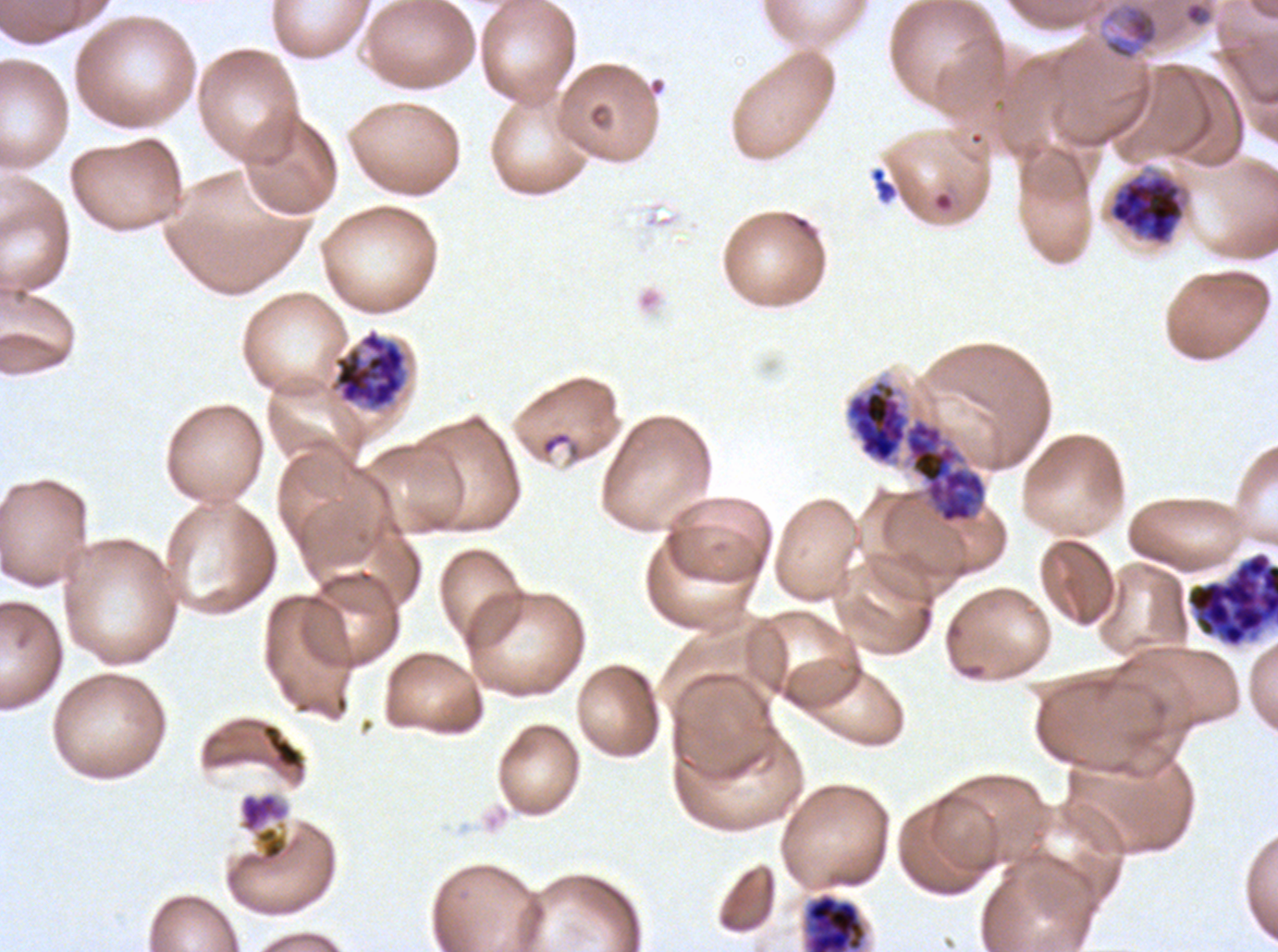 Approximate bounding boxes as (x1, y1, x2, y2) in pixels. Segmenter locations: (1185, 550, 1277, 650). Early schizont locations: (847, 380, 987, 523), (239, 792, 288, 833). Ring locations: (1185, 2, 1208, 24), (870, 167, 896, 201). Late schizont locations: (1106, 166, 1191, 247), (328, 327, 409, 412), (847, 380, 987, 523) (two touching objects share this one region), (804, 893, 867, 951). Mid trophozoite locations: (1099, 1, 1161, 62). Debris locations: (262, 723, 302, 768). Image is 1278×952 pixels. Thin blood film. Plasmodium falciparum from a patient in The Gambia, cultured ex vivo for 24 to 48 hours. Life-cycle stages observed: ring, mid trophozoite, early schizont, late schizont, segmenter. One sub-image of a larger composite. Giemsa-stained preparation.